Report the malaria status of this cell.
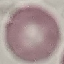
It is uninfected.

Summary:
  - Preparation: thin blood smear
  - Stain: Giemsa
  - Capture: smartphone camera at the microscope eyepiece
  - Image type: cell patch, automatically extracted from a larger field of view and resized to 64 × 64 pixels